Name the parasite shown.
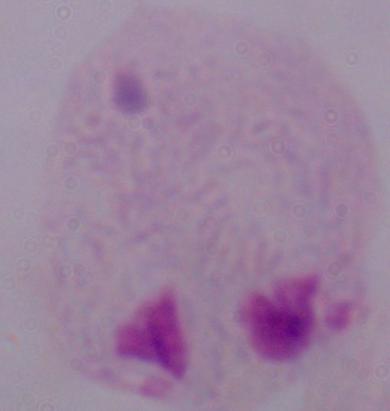

This is a trichomonad.

magnification = 1000x
modality = photomicrograph